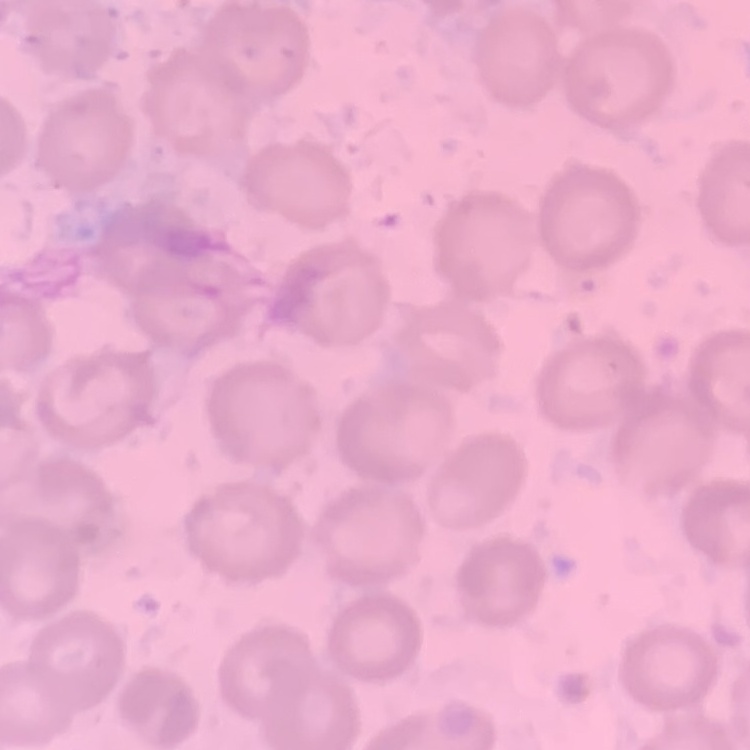

{
  "erythrocyte_morphology": "no rouleaux formation",
  "stain": "Field's or Giemsa",
  "preparation": "thin peripheral smear",
  "image_type": "square crop of a larger photomicrograph"
}